State which parasite is depicted.
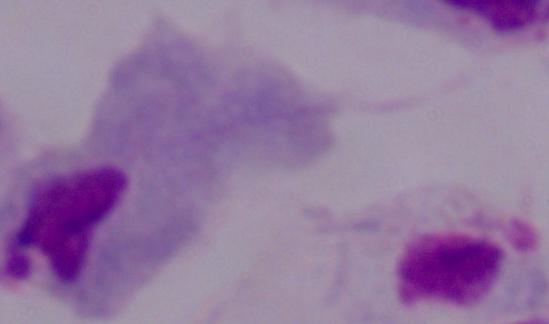

This is a trichomonad.

Photomicrograph. 1000x magnification.